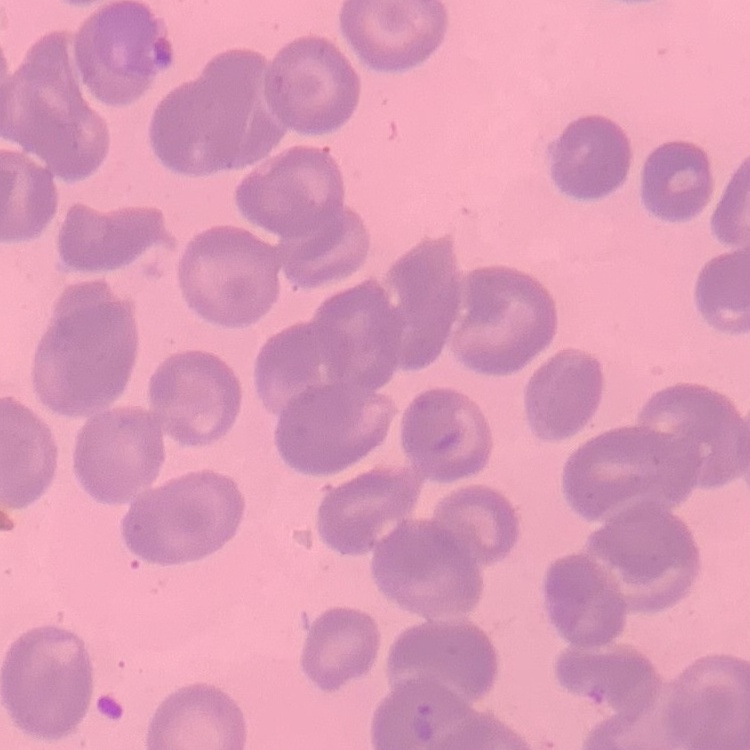
The erythrocytes exhibit no rouleaux formation. Square crop of a larger photomicrograph. Thin peripheral smear. Stained with either Field's or Giemsa.